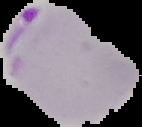 Result: malaria parasites detected. From a thin blood smear. Image is 142×127 pixels. Cell region segmented out of the field of view; the surrounding area is masked to black.